Locate every uninfected red blood cell.
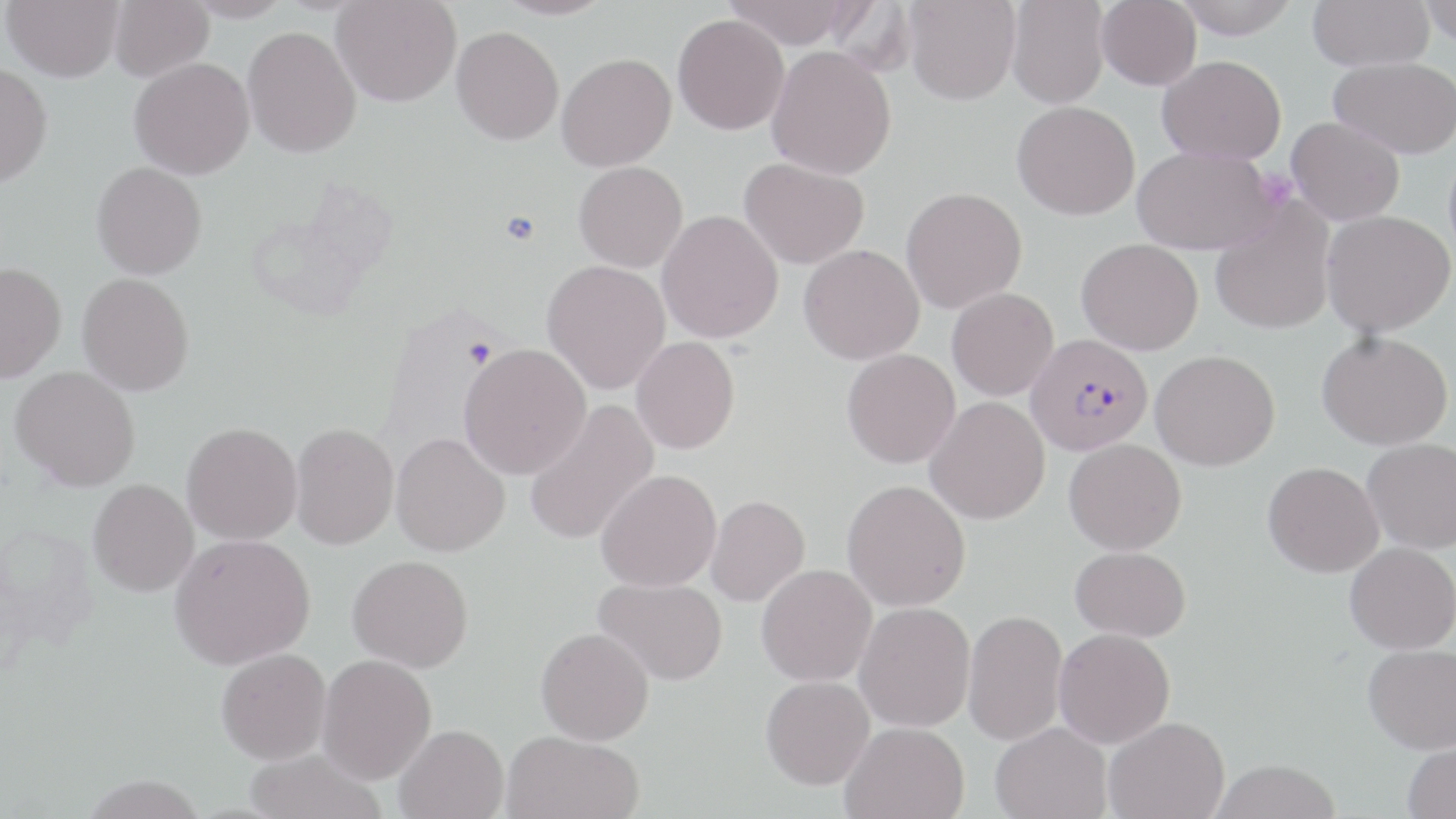

Approximate bounding boxes as (x1, y1, x2, y2) in pixels.
Uninfected red blood cells: (2, 0, 124, 83), (109, 0, 214, 83), (182, 0, 292, 23), (331, 0, 461, 107), (493, 0, 615, 20), (723, 0, 860, 49), (904, 0, 1021, 105), (1006, 0, 1109, 109), (1097, 0, 1201, 90), (1173, 0, 1300, 38), (1307, 0, 1434, 71), (1418, 0, 1455, 47), (672, 14, 789, 135), (242, 25, 361, 158), (451, 26, 564, 145), (766, 45, 897, 180), (556, 53, 676, 171), (1157, 55, 1287, 164), (128, 56, 255, 179), (1329, 56, 1456, 159), (0, 63, 53, 190), (1012, 101, 1140, 220), (1286, 116, 1405, 225), (1132, 145, 1279, 255), (738, 157, 870, 269), (91, 161, 207, 280), (573, 161, 688, 272), (900, 187, 1027, 313), (1210, 201, 1335, 335), (657, 209, 784, 343), (1321, 209, 1456, 337), (1076, 238, 1203, 355), (798, 244, 925, 365), (541, 260, 671, 394), (0, 262, 66, 383), (77, 272, 194, 396), (947, 287, 1058, 400), (1316, 330, 1453, 450), (630, 336, 740, 455), (459, 343, 591, 479), (841, 348, 960, 468), (1150, 350, 1280, 471), (9, 366, 140, 491), (925, 396, 1050, 524), (522, 399, 659, 546), (181, 422, 303, 546), (290, 422, 399, 549), (390, 432, 509, 556), (1362, 437, 1456, 553), (1064, 438, 1187, 554), (1263, 461, 1384, 577), (595, 469, 722, 592), (88, 479, 199, 596), (841, 479, 971, 611), (706, 494, 810, 606), (169, 533, 316, 669), (1344, 542, 1456, 654), (1071, 546, 1191, 641), (348, 554, 473, 672), (756, 564, 877, 686), (593, 577, 728, 685), (855, 602, 976, 732), (963, 609, 1068, 746), (535, 627, 654, 745), (1054, 628, 1175, 748), (1363, 644, 1456, 753), (216, 647, 331, 764), (317, 654, 436, 784), (760, 675, 875, 790), (1104, 716, 1230, 819), (840, 721, 969, 818), (990, 721, 1112, 819), (394, 724, 509, 819), (502, 730, 644, 819), (1402, 739, 1456, 819), (244, 748, 385, 819), (1209, 759, 1342, 819).

Summary:
  - Plasmodium falciparum-infected red blood cell locations: (1025, 333, 1153, 456)
  - Platelet locations: (1257, 169, 1298, 210), (498, 210, 543, 246)
  - Slide-level diagnosis: Plasmodium falciparum
  - Modality: light microscopy
  - Image size: 1456×819 pixels
  - Field of view: single
  - Magnification: 1000x
  - Stain: May-Grünwald-Giemsa
  - Preparation: thin blood smear